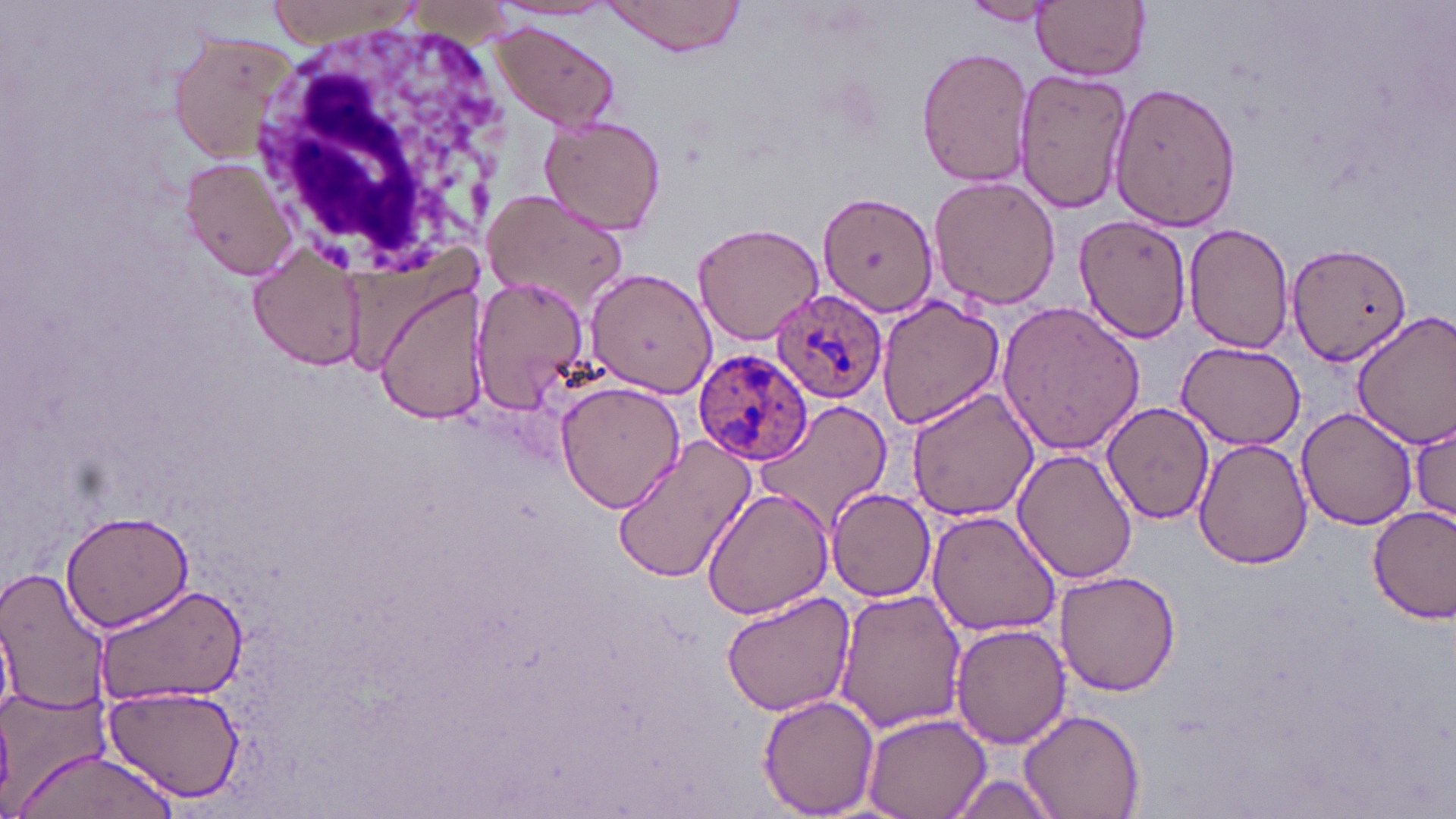

Approximate bounding boxes as (x1, y1, x2, y2) in pixels. Uninfected red blood cell locations: (264, 0, 427, 47), (601, 0, 746, 57), (1032, 0, 1150, 80), (959, 1, 1063, 26), (487, 22, 624, 129), (165, 27, 304, 165), (915, 48, 1032, 186), (1013, 65, 1134, 217), (1109, 81, 1244, 228), (539, 113, 666, 236), (181, 155, 299, 282), (928, 173, 1062, 308), (483, 189, 631, 314), (820, 191, 939, 319), (1075, 213, 1193, 345), (691, 220, 824, 344), (1184, 222, 1297, 353), (1287, 240, 1413, 367), (247, 244, 368, 374), (583, 267, 715, 399), (468, 273, 590, 413), (374, 279, 490, 423), (875, 296, 1005, 429), (996, 299, 1147, 456), (1352, 311, 1456, 448), (1178, 342, 1305, 449), (555, 379, 687, 514), (903, 386, 1041, 523), (755, 399, 894, 533), (1102, 400, 1214, 524), (1296, 407, 1419, 532), (1411, 414, 1455, 528), (612, 435, 760, 585), (1193, 438, 1314, 569), (1013, 447, 1139, 585), (700, 487, 835, 620), (827, 488, 935, 602), (1368, 507, 1456, 623), (59, 508, 197, 631), (926, 511, 1061, 638), (0, 568, 115, 716), (1055, 570, 1182, 697), (94, 585, 249, 702), (834, 587, 969, 732), (721, 589, 857, 717), (950, 625, 1071, 750), (101, 682, 244, 803), (0, 685, 111, 809), (759, 694, 879, 816), (1020, 707, 1145, 818), (863, 711, 991, 818), (11, 747, 182, 817), (944, 771, 1061, 817). White blood cell locations: (257, 19, 516, 279). Plasmodium ovale-infected red blood cell locations: (769, 287, 888, 405), (693, 348, 814, 464). Slide-level diagnosis: Plasmodium ovale. Optical microscopy. Image is 1456×819 pixels. 1000x magnification. May-Grünwald-Giemsa stain. Single field of view. Thin blood film.